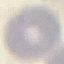
result = no malaria parasites seen
image type = cell patch, automatically extracted from a larger field of view and resized to 64 × 64 pixels
capture = smartphone through the microscope eyepiece
stain = Giemsa
preparation = thin smear